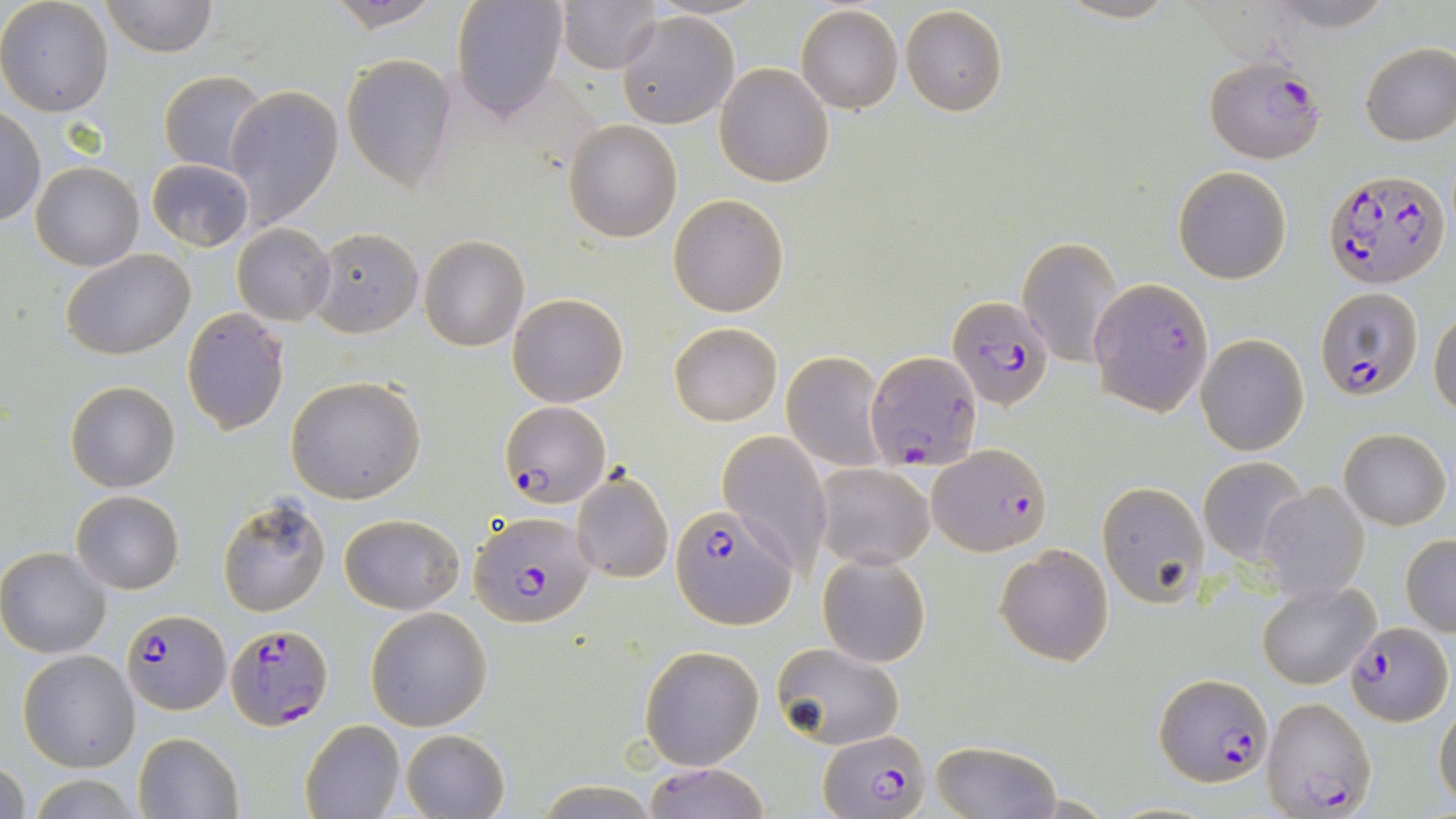
Summary:
  - Coordinate format: approximate bounding boxes as [x1, y1, x2, y2] in pixels
  - Uninfected red blood cell locations: [98, 0, 217, 57], [326, 0, 443, 32], [450, 0, 570, 119], [1263, 0, 1396, 32], [0, 1, 115, 118], [557, 1, 663, 74], [795, 4, 902, 115], [899, 6, 1008, 115], [616, 10, 739, 129], [1359, 42, 1456, 147], [342, 54, 459, 192], [714, 63, 833, 187], [158, 71, 267, 174], [225, 87, 343, 228], [0, 109, 44, 226], [565, 119, 682, 242], [147, 158, 254, 252], [31, 162, 144, 270], [1173, 165, 1291, 285], [668, 192, 790, 317], [231, 223, 334, 325], [308, 227, 423, 337], [1019, 235, 1121, 367], [419, 236, 529, 352], [62, 248, 195, 359], [507, 293, 629, 408], [181, 308, 291, 435], [1429, 310, 1456, 420], [668, 323, 784, 424], [1195, 333, 1310, 455], [783, 350, 888, 471], [284, 376, 426, 504], [65, 381, 180, 492], [1339, 429, 1451, 529], [717, 430, 834, 572], [1198, 455, 1308, 566], [814, 464, 934, 570], [571, 471, 675, 585], [1095, 481, 1207, 606], [1258, 481, 1370, 601], [71, 490, 184, 594], [217, 494, 331, 617], [339, 512, 466, 616], [1401, 534, 1456, 636], [994, 544, 1114, 666], [0, 546, 114, 658], [817, 551, 932, 668], [1256, 580, 1379, 689], [365, 607, 492, 731], [773, 641, 903, 750], [639, 645, 763, 769], [17, 649, 140, 772], [1432, 702, 1456, 807], [300, 719, 405, 819], [400, 729, 509, 818], [133, 732, 244, 818], [930, 742, 1061, 818], [1, 754, 28, 819], [641, 761, 770, 819], [20, 772, 152, 819], [531, 782, 662, 815]
  - Plasmodium falciparum-infected red blood cell locations: [1206, 58, 1326, 166], [1325, 168, 1450, 290], [1092, 281, 1212, 418], [1315, 289, 1420, 403], [949, 294, 1055, 411], [869, 351, 981, 470], [499, 400, 611, 506], [928, 444, 1051, 556], [671, 505, 797, 630], [468, 510, 594, 628], [121, 607, 228, 714], [1346, 621, 1452, 727], [225, 623, 331, 730], [1158, 676, 1276, 788], [1262, 696, 1375, 819], [817, 730, 933, 817]
  - Slide-level diagnosis: Plasmodium falciparum
  - Stain: May-Grünwald-Giemsa
  - Magnification: 1000x
  - Preparation: thin blood film
  - Modality: light microscopy
  - Field of view: one of a larger specimen
  - Image size: 1456×819 pixels